Locate every blood parasite and identify its species.
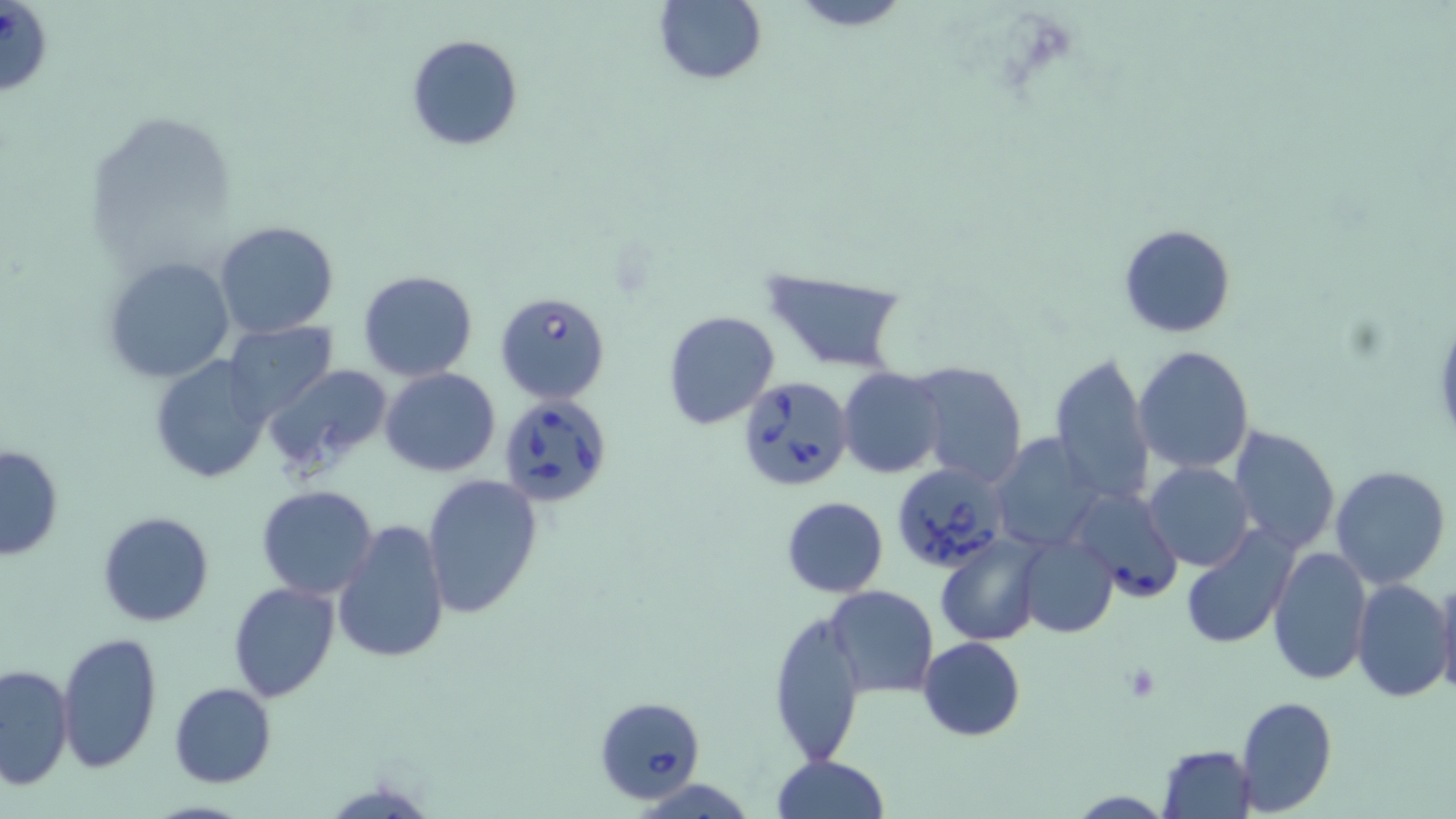

Approximate bounding boxes as (x1,y1)-(x2,y2) corner pairs in pixels.
Babesia divergens-infected red blood cells: (493,290)-(612,404), (737,377)-(854,493), (498,396)-(615,509), (889,462)-(1013,576), (1065,488)-(1183,602), (592,695)-(705,803).
No Plasmodium falciparum, Plasmodium ovale, Plasmodium malariae, Plasmodium vivax, or Trypanosoma brucei observed.

Summary:
  - Uninfected red blood cell locations: (785,0)-(919,31), (652,1)-(768,86), (405,33)-(523,152), (213,220)-(340,339), (1118,224)-(1237,337), (102,256)-(234,382), (758,267)-(909,373), (358,271)-(479,382), (663,309)-(780,430), (222,321)-(338,423), (1133,344)-(1255,473), (1049,350)-(1156,507), (148,355)-(272,485), (910,359)-(1027,489), (260,363)-(396,480), (838,367)-(948,478), (379,368)-(501,477), (1228,425)-(1341,555), (991,433)-(1104,553), (1,443)-(65,562), (1142,461)-(1255,571), (1330,464)-(1452,588), (421,471)-(544,619), (256,484)-(381,600), (780,496)-(888,598), (96,511)-(216,626), (333,521)-(450,666), (1179,525)-(1297,651), (1017,534)-(1119,639), (935,535)-(1045,646), (1267,546)-(1371,686), (1435,577)-(1456,701), (1352,579)-(1454,702), (228,581)-(340,701), (824,585)-(939,700), (769,607)-(866,765), (56,631)-(162,774), (918,636)-(1025,741), (1,663)-(75,790), (169,681)-(276,787), (1234,694)-(1336,816), (1157,743)-(1258,818), (770,755)-(890,818)
  - Slide-level diagnosis: Babesia divergens
  - Magnification: 1000x
  - Field of view: single
  - Image size: 1456×819 pixels
  - Preparation: thin blood smear
  - Stain: May-Grünwald-Giemsa
  - Modality: light microscopy